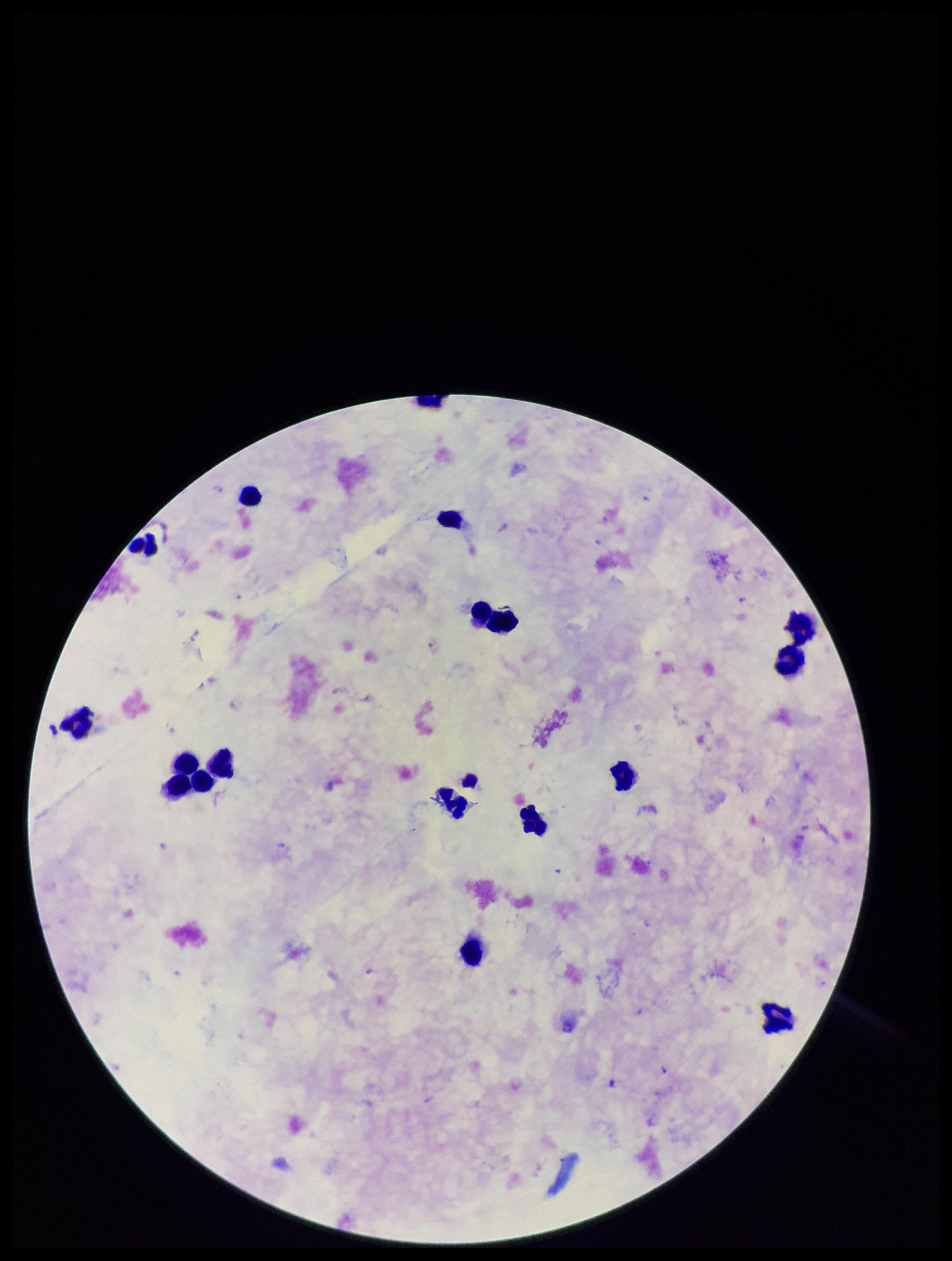

Summary:
  - Plasmodium parasites: seen
  - Preparation: thick smear
  - Patient malaria status: infected
  - Image size: 952×1261 pixels
  - Field of view: one from this slide
  - Leukocyte count: 15
  - Species reported for this patient: Plasmodium falciparum
  - Stain: Giemsa
  - Capture: smartphone photograph through the microscope eyepiece
  - Parasite count: 15